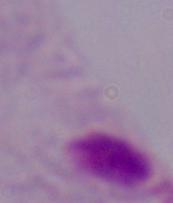

Summary:
  - Modality: photomicrograph
  - Magnification: 1000x
  - Identification: trichomonad